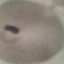 Result: malaria parasites detected. Thin blood smear. Acquired by smartphone through the microscope eyepiece. Giemsa-stained preparation. Automatically extracted cell patch, resized to 64 × 64 pixels.